Assess this cell for malaria.
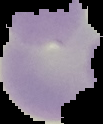

Uninfected.

preparation = thin blood film
image size = 103×124 pixels
image type = cell region segmented out of the field of view; surrounding area masked to black